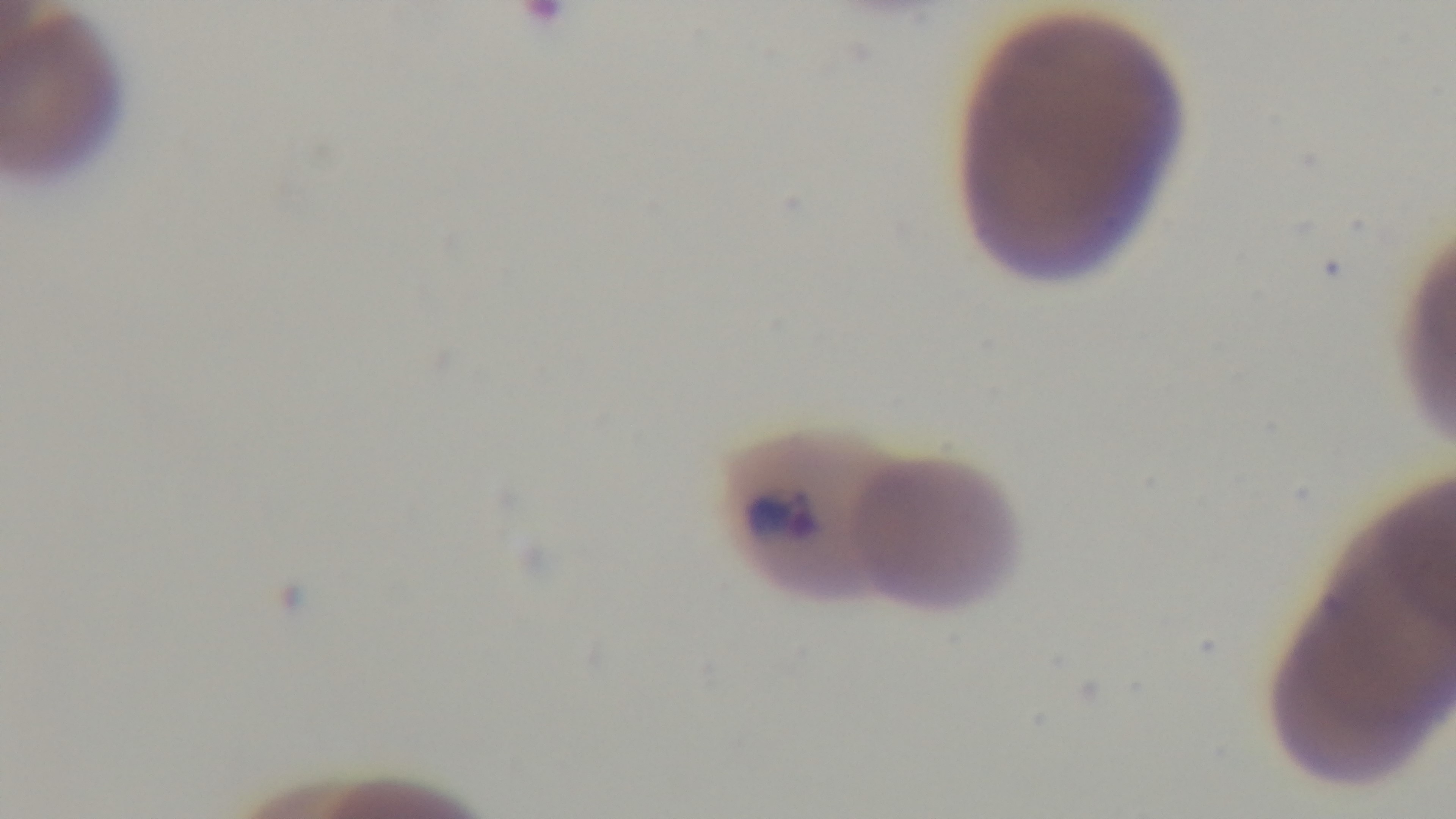

{
  "field_of_view": "single",
  "capture": "mounted 4K digital camera",
  "modality": "light microscopy",
  "malaria_status": "infected",
  "objective": "100x oil immersion",
  "stain": "Giemsa",
  "preparation": "thin blood film"
}